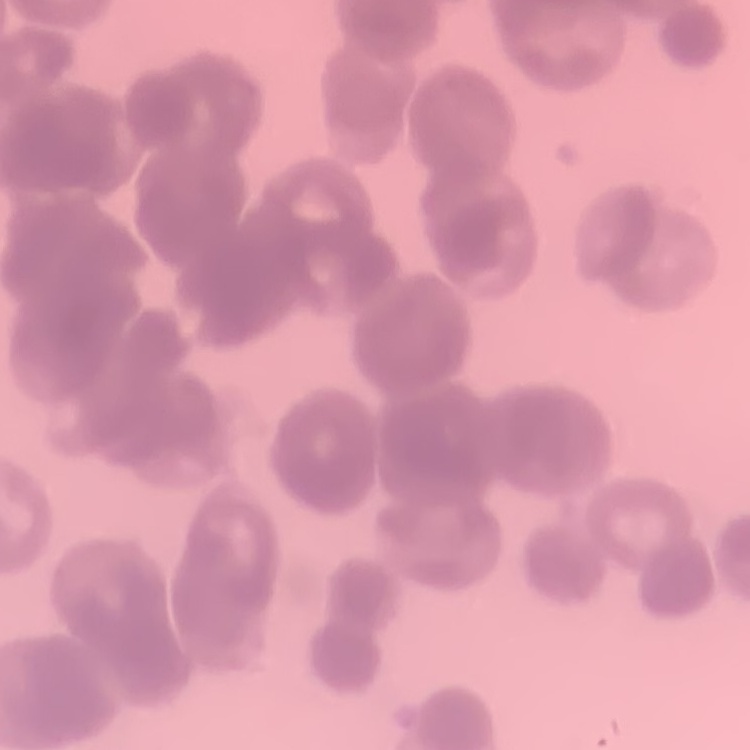
erythrocyte_morphology: rouleaux formation
preparation: thin blood film
image_type: square crop of a larger photomicrograph
stain: Field's or Giemsa